Outline platelets.
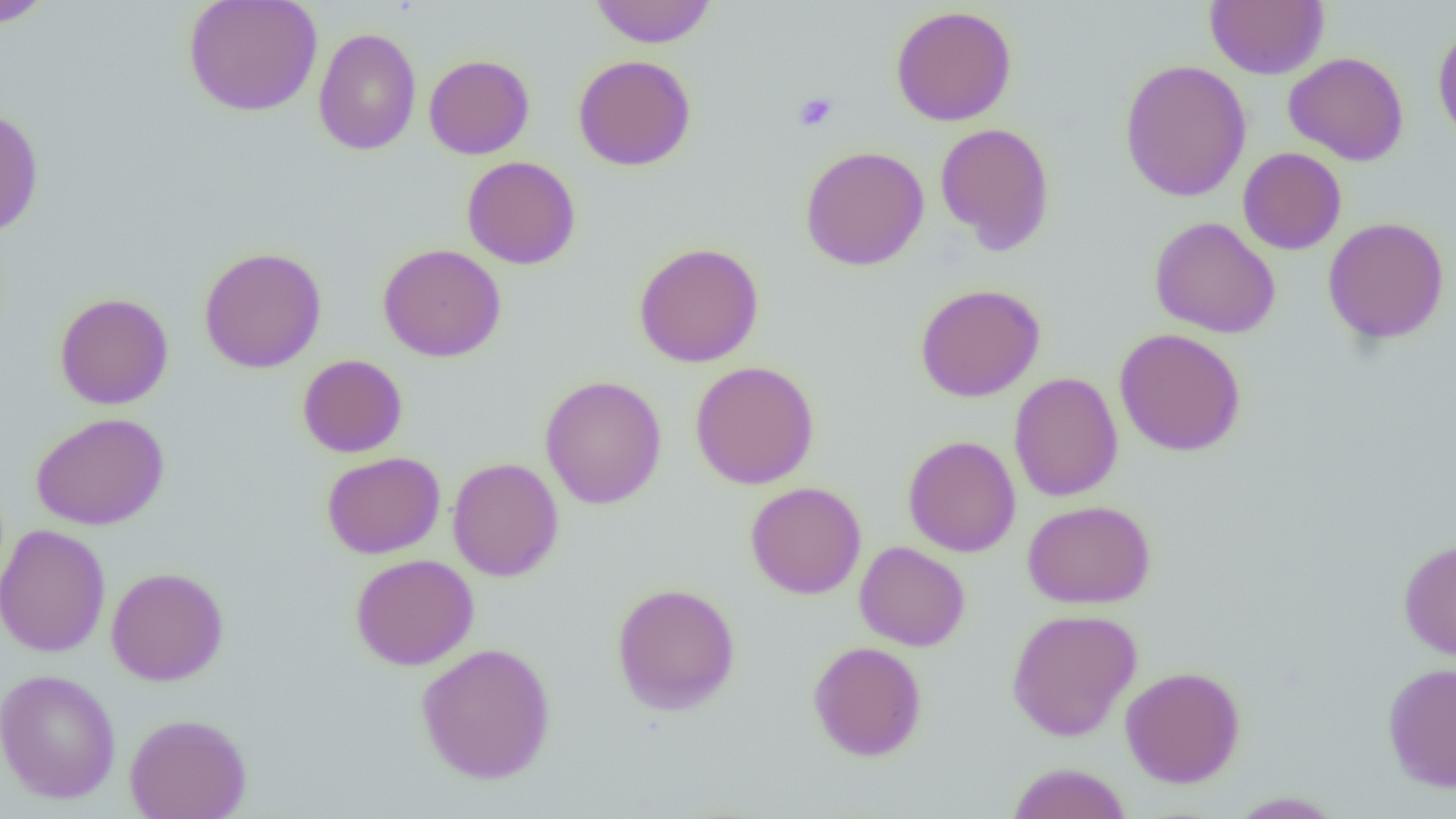
Approximate bounding boxes as (x1, y1, x2, y2) in pixels.
Platelets: (794, 92, 837, 131).

Uninfected red blood cell locations: (1, 0, 53, 27), (183, 0, 322, 116), (589, 0, 718, 48), (1204, 0, 1329, 80), (890, 5, 1017, 126), (1432, 22, 1456, 147), (313, 27, 422, 155), (1283, 51, 1409, 166), (423, 54, 535, 159), (573, 55, 696, 171), (1119, 59, 1252, 202), (0, 107, 44, 237), (934, 122, 1055, 254), (799, 145, 929, 271), (1237, 147, 1347, 255), (462, 156, 581, 269), (1149, 216, 1281, 339), (1322, 217, 1450, 344), (634, 241, 764, 367), (377, 243, 506, 362), (198, 247, 327, 373), (915, 283, 1045, 402), (54, 292, 173, 410), (1114, 328, 1246, 456), (297, 354, 408, 457), (689, 360, 819, 490), (1008, 372, 1123, 502), (540, 375, 667, 509), (30, 412, 169, 531), (903, 435, 1020, 557), (321, 451, 445, 559), (447, 457, 564, 582), (745, 482, 866, 599), (1022, 499, 1156, 609), (0, 523, 111, 658), (1398, 537, 1456, 660), (854, 541, 971, 651), (350, 554, 479, 670), (106, 566, 229, 686), (611, 582, 741, 715), (1005, 608, 1142, 741), (807, 641, 927, 761), (416, 642, 556, 785), (1383, 662, 1456, 792), (1120, 666, 1246, 788), (0, 668, 121, 804), (124, 712, 252, 819), (1005, 762, 1132, 819), (1226, 791, 1346, 818). Slide-level diagnosis: negative for blood parasites. Image is 1456×819 pixels. Single field of view. Thin blood smear. Captured at 1000x magnification. Light microscopy.